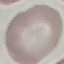
Summary:
  - Result: no malaria parasites seen
  - Image type: cell patch, automatically extracted from a larger field of view and resized to 64 × 64 pixels
  - Stain: Giemsa
  - Preparation: thin blood smear
  - Capture: smartphone camera at the microscope eyepiece